Assess the morphology of the erythrocytes.
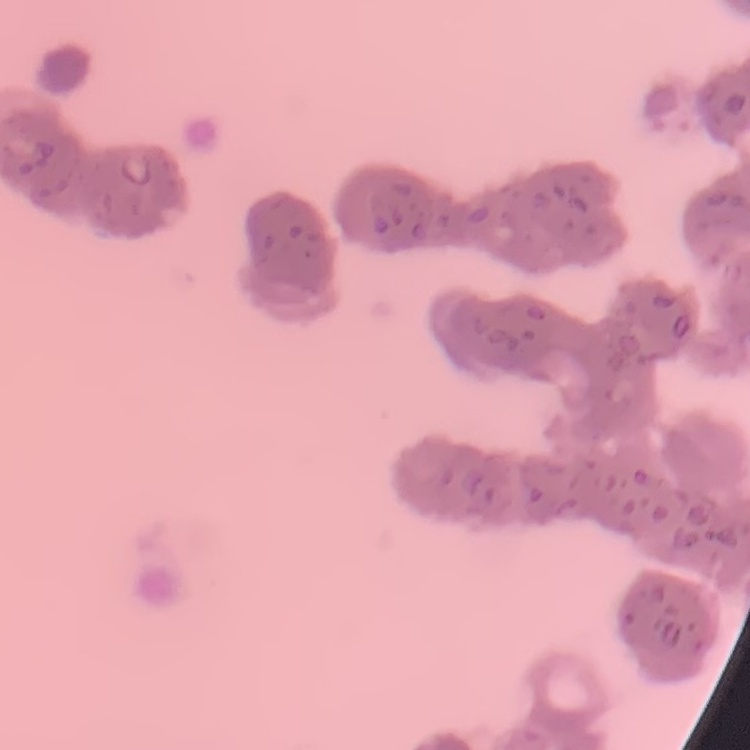

They show rouleaux formation.

Summary:
  - Stain: Field's or Giemsa
  - Image type: square crop of a larger photomicrograph
  - Preparation: thin blood film